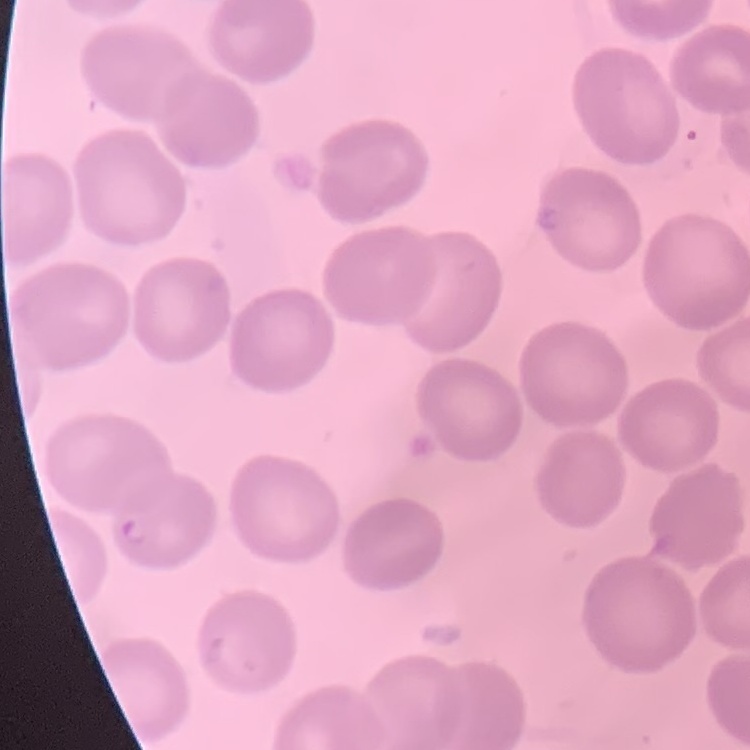
erythrocyte morphology = no rouleaux formation
preparation = thin blood film
stain = Field's or Giemsa
image type = one tile cut from a larger photomicrograph